State which parasite is depicted.
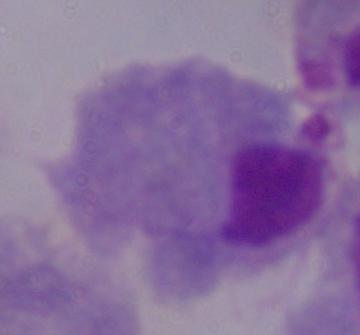

This is a trichomonad.

modality = photomicrograph
magnification = 1000x